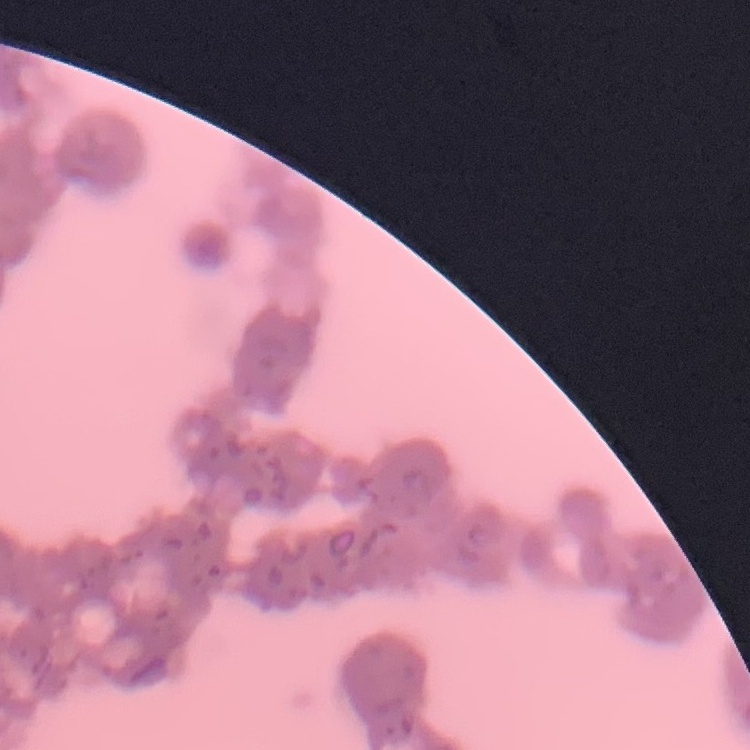
Summary:
  - Erythrocyte morphology: rouleaux formation
  - Image type: square crop of a larger photomicrograph
  - Preparation: thin peripheral smear
  - Stain: Field's or Giemsa